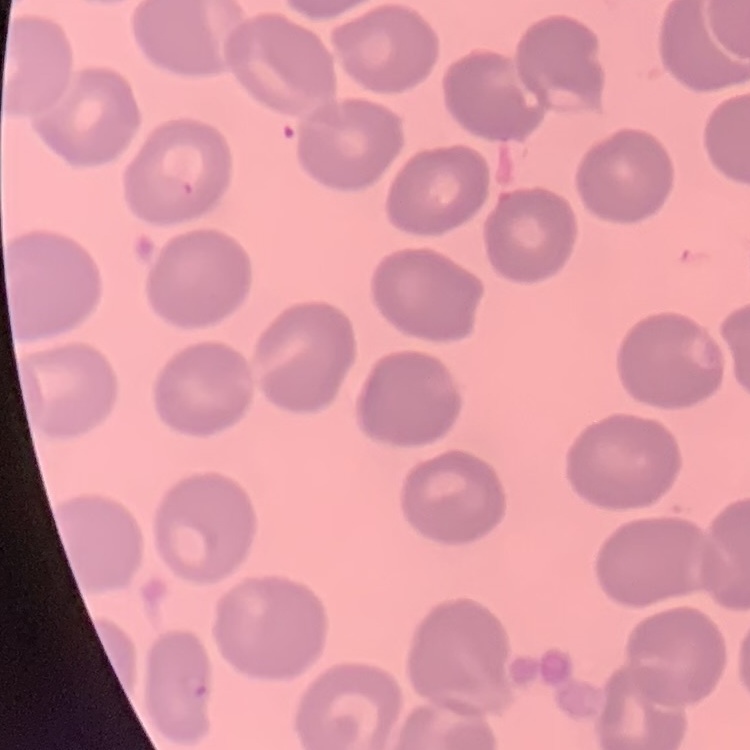
red blood cell morphology = no rouleaux formation
preparation = thin blood smear
image type = one tile cut from a larger photomicrograph
stain = Field's or Giemsa